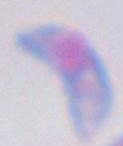

magnification = 1000x
identification = Toxoplasma gondii
modality = photomicrograph